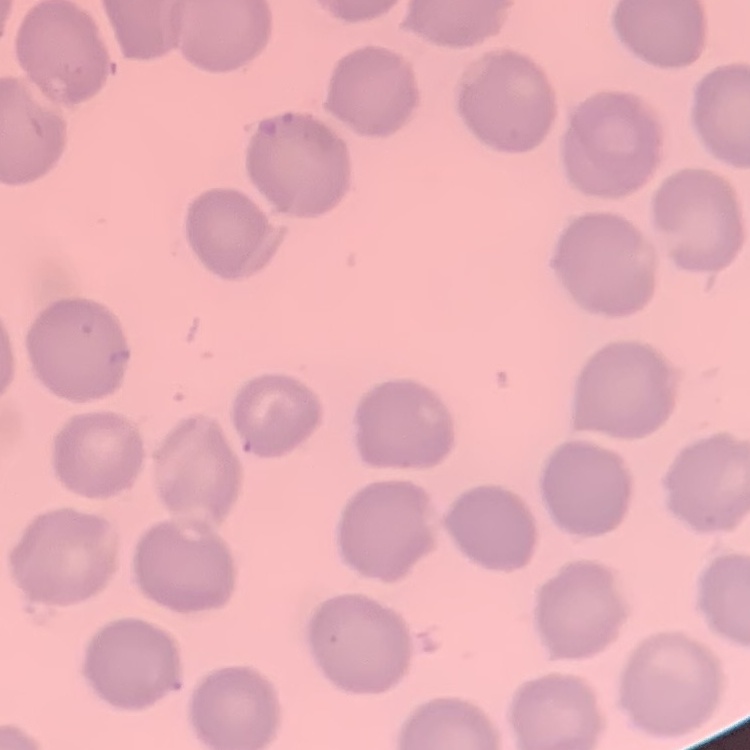

erythrocyte morphology = no rouleaux formation
preparation = thin blood film
stain = Field's or Giemsa
image type = one tile cut from a larger photomicrograph